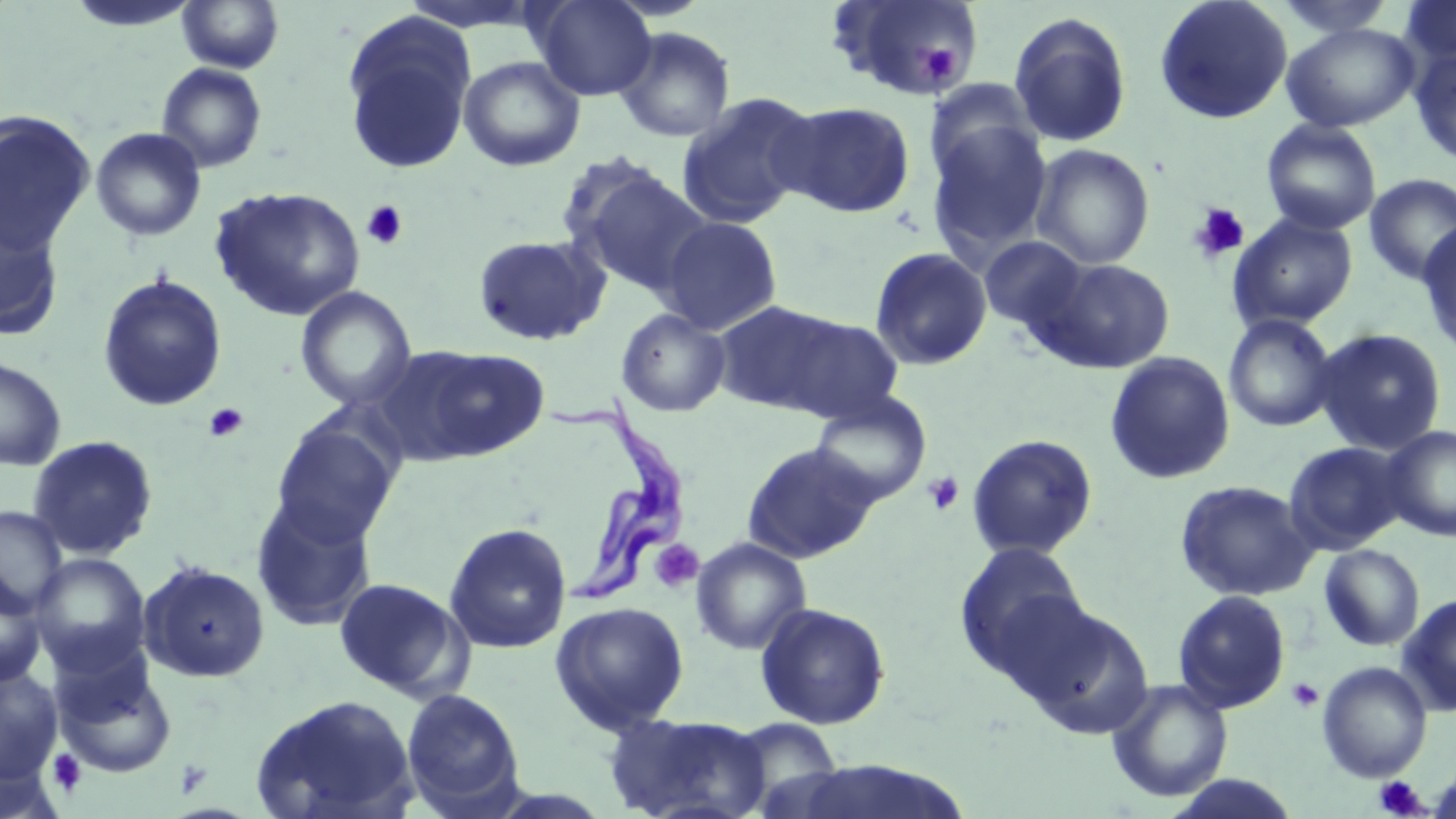

Summary:
  - Coordinate format: approximate bounding boxes as (x1, y1, x2, y2) in pixels
  - Platelet locations: (922, 43, 960, 85), (361, 201, 408, 250), (1188, 202, 1250, 263), (203, 402, 250, 442), (922, 471, 965, 516), (649, 539, 704, 593), (1286, 678, 1324, 713), (49, 749, 88, 796), (1374, 776, 1429, 817)
  - Trypanosoma brucei locations: (546, 383, 694, 612)
  - Uninfected red blood cell locations: (176, 0, 284, 73), (531, 0, 656, 101), (829, 0, 983, 101), (1154, 0, 1293, 125), (1402, 0, 1456, 69), (64, 1, 200, 33), (1272, 1, 1399, 38), (1009, 11, 1132, 148), (340, 12, 478, 175), (1281, 23, 1419, 133), (613, 26, 736, 143), (1410, 47, 1456, 167), (458, 56, 585, 171), (156, 62, 267, 173), (924, 80, 1041, 186), (677, 91, 820, 227), (775, 100, 916, 218), (0, 111, 96, 254), (1261, 120, 1381, 235), (926, 122, 1052, 261), (90, 127, 207, 242), (1030, 144, 1155, 269), (566, 162, 711, 296), (1363, 174, 1456, 286), (210, 186, 365, 321), (0, 206, 65, 341), (1228, 214, 1358, 331), (658, 215, 783, 336), (1416, 221, 1456, 358), (472, 234, 610, 346), (979, 235, 1089, 333), (869, 246, 993, 371), (1037, 258, 1175, 373), (96, 274, 228, 412), (295, 286, 417, 412), (737, 306, 906, 423), (615, 308, 731, 417), (1224, 314, 1338, 432), (1312, 328, 1448, 455), (406, 346, 551, 461), (1104, 352, 1236, 485), (0, 356, 67, 471), (809, 392, 932, 508), (270, 420, 401, 547), (1381, 425, 1456, 542), (966, 434, 1098, 560), (26, 435, 159, 560), (743, 441, 879, 564), (1284, 441, 1411, 554), (1174, 480, 1319, 602), (251, 496, 379, 632), (0, 505, 68, 617), (443, 522, 572, 654), (690, 536, 812, 656), (953, 541, 1090, 688), (1318, 544, 1424, 651), (28, 552, 151, 675), (138, 560, 270, 683), (0, 571, 47, 690), (332, 577, 472, 702), (1172, 590, 1291, 714), (1397, 593, 1456, 716), (549, 601, 690, 735), (755, 602, 891, 729), (1020, 602, 1155, 740), (52, 652, 177, 778), (1317, 660, 1433, 782), (0, 667, 62, 784), (1106, 678, 1233, 803), (400, 688, 526, 815), (250, 693, 420, 819), (604, 712, 772, 819), (724, 717, 846, 812), (786, 760, 972, 818), (1164, 774, 1302, 818)
  - Slide-level diagnosis: Trypanosoma brucei
  - Image size: 1456×819 pixels
  - Stain: May-Grünwald-Giemsa
  - Field of view: single
  - Preparation: thin blood smear
  - Modality: optical microscopy
  - Magnification: 1000x